Identify the cell.
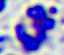
A leukocyte.

Photomicrograph. 400x magnification.